Classify this cell by malaria status.
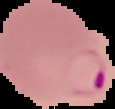

Parasitized.

image size = 115×109 pixels
preparation = thin blood smear
image type = segmented cell region on a black background